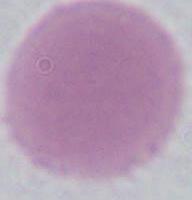
Summary:
  - Modality: micrograph
  - Identification: erythrocyte
  - Magnification: 1000x